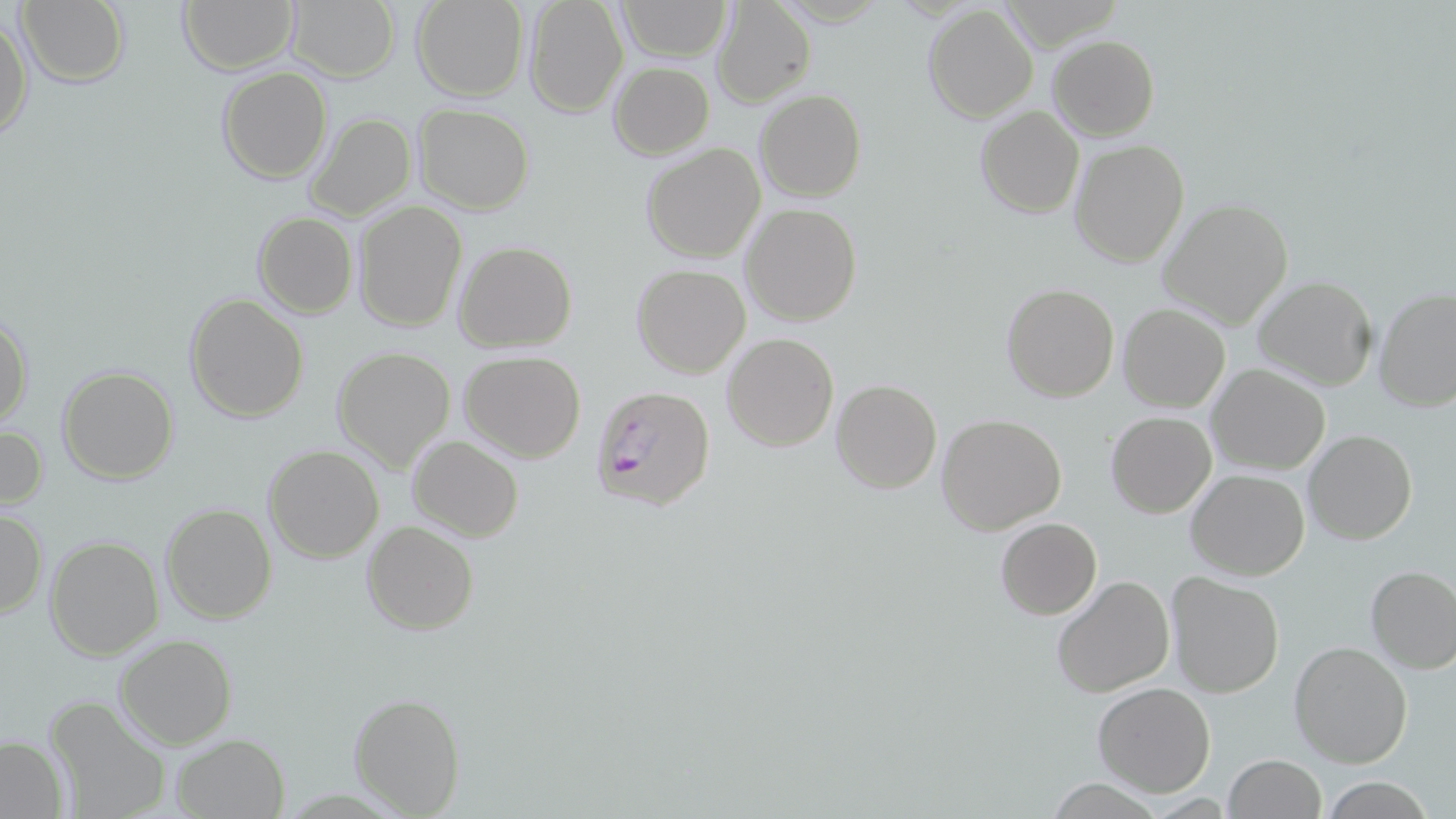
Approximate bounding boxes as [x1, y1, x2, y2] in pixels. Uninfected red blood cell locations: [15, 0, 129, 88], [178, 0, 298, 74], [412, 0, 528, 101], [523, 0, 628, 117], [615, 0, 731, 61], [711, 0, 815, 108], [287, 1, 399, 81], [922, 5, 1039, 124], [0, 13, 33, 140], [1048, 35, 1160, 141], [609, 63, 713, 158], [216, 66, 334, 184], [755, 90, 866, 202], [413, 103, 534, 214], [975, 104, 1084, 218], [304, 111, 416, 221], [1068, 139, 1189, 268], [641, 143, 765, 263], [1157, 198, 1295, 330], [352, 201, 468, 333], [740, 202, 861, 325], [251, 211, 358, 317], [455, 242, 577, 350], [632, 263, 750, 378], [1252, 275, 1380, 392], [1000, 282, 1119, 402], [1373, 286, 1456, 412], [185, 294, 310, 424], [1117, 303, 1231, 413], [0, 308, 32, 431], [722, 332, 839, 452], [332, 344, 456, 472], [459, 351, 586, 461], [57, 365, 180, 482], [1206, 365, 1331, 475], [831, 380, 942, 494], [1106, 411, 1216, 518], [937, 414, 1067, 535], [0, 424, 48, 514], [1304, 429, 1417, 545], [409, 435, 524, 541], [262, 445, 385, 564], [1185, 469, 1310, 581], [160, 501, 275, 623], [1, 509, 46, 617], [995, 518, 1102, 619], [361, 520, 480, 634], [45, 536, 163, 659], [1365, 564, 1456, 672], [1165, 571, 1285, 697], [1051, 573, 1176, 698], [115, 634, 236, 749], [1289, 641, 1412, 768], [1092, 682, 1217, 798], [349, 691, 463, 815], [44, 692, 173, 819], [171, 734, 290, 818], [0, 736, 68, 817], [1222, 754, 1326, 819], [1319, 775, 1434, 818]. Plasmodium falciparum-infected red blood cell locations: [588, 384, 716, 513]. Slide-level diagnosis: Plasmodium falciparum. Thin blood smear. One field of a larger specimen. Image is 1456×819 pixels. May-Grünwald-Giemsa stain. 1000x magnification. Light microscopy.